Classify this cell by malaria status.
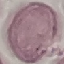

Uninfected.

capture = smartphone through the microscope eyepiece
preparation = thin smear
image type = cell patch, automatically extracted from a larger field of view and resized to 64 × 64 pixels
stain = Giemsa